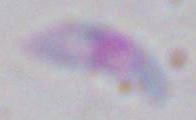
identification = Toxoplasma gondii
modality = photomicrograph
magnification = 1000x